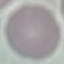
Result: negative for malaria parasites. Cell patch, automatically extracted from a larger field of view and resized to 64 × 64 pixels. Giemsa stain. Acquired by smartphone through the microscope eyepiece. Thin smear of blood.